Assess this cell for malaria.
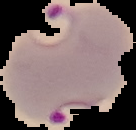

Parasitized.

Summary:
  - Preparation: thin blood smear
  - Image type: segmented cell region on a black background
  - Image size: 136×130 pixels